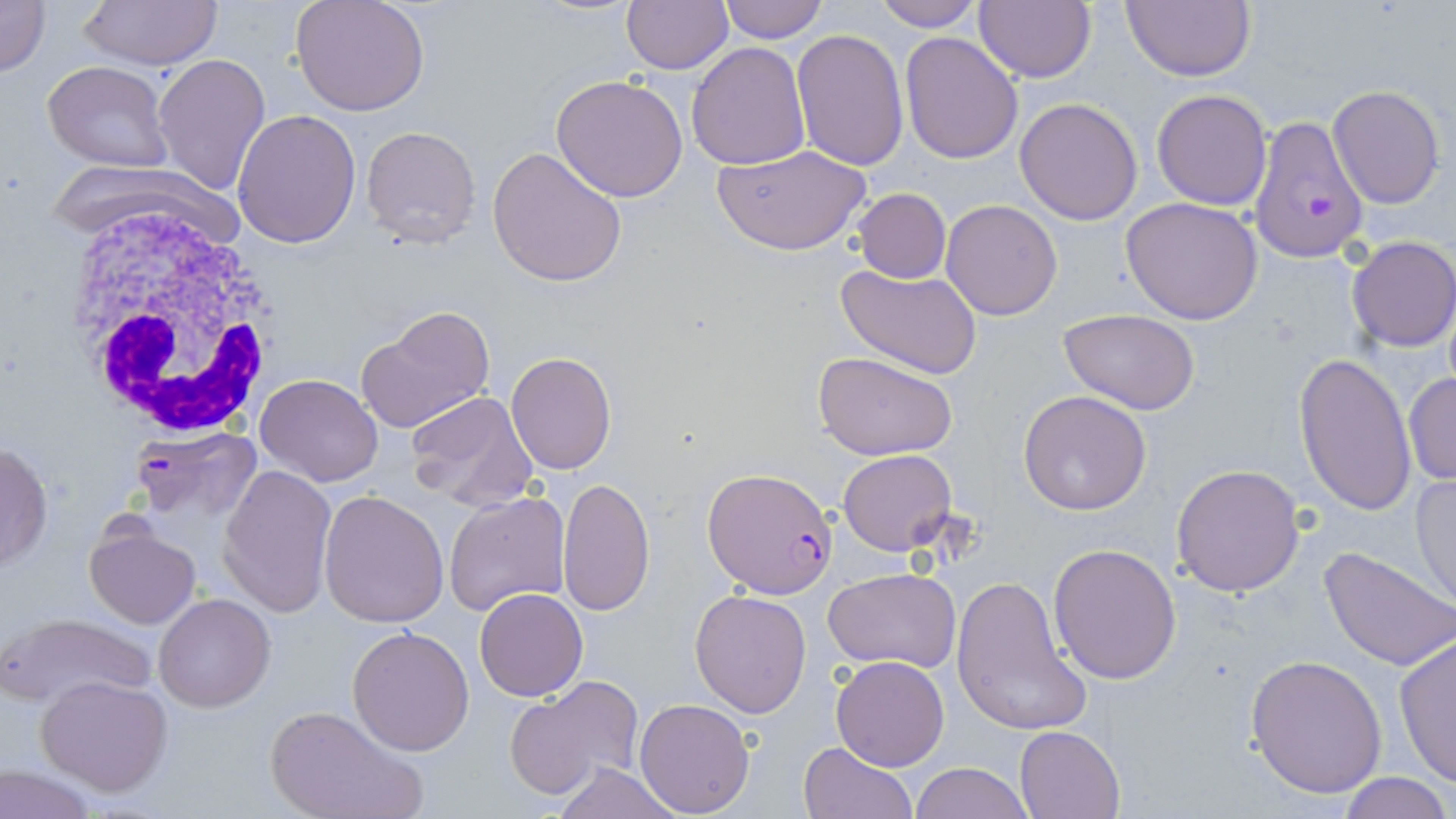

Summary:
  - Coordinate format: approximate bounding boxes as (x1,y1)-(x2,y2) corner pairs in pixels
  - White blood cell locations: (56,198)-(289,446)
  - Plasmodium falciparum-infected red blood cell locations: (1236,118)-(1367,261), (131,427)-(262,526), (702,465)-(839,599)
  - Uninfected red blood cell locations: (0,0)-(50,77), (77,0)-(221,70), (621,0)-(733,73), (716,0)-(832,44), (1123,0)-(1256,82), (291,1)-(431,116), (873,1)-(983,31), (975,2)-(1096,83), (791,29)-(909,170), (900,32)-(1023,164), (686,42)-(812,170), (152,54)-(272,197), (42,59)-(173,171), (550,75)-(689,202), (1327,84)-(1446,211), (1151,89)-(1272,210), (1015,97)-(1144,224), (232,110)-(362,249), (360,126)-(482,248), (712,142)-(872,256), (487,145)-(625,287), (852,187)-(951,285), (1121,196)-(1263,323), (940,199)-(1064,320), (1346,237)-(1456,353), (836,264)-(983,381), (355,308)-(496,435), (1059,309)-(1204,415), (812,350)-(959,459), (507,352)-(616,474), (1294,353)-(1418,518), (1402,373)-(1455,486), (255,374)-(384,487), (1018,389)-(1153,515), (405,390)-(540,510), (0,441)-(53,574), (837,449)-(957,556), (1172,462)-(1306,596), (218,465)-(337,617), (1409,472)-(1456,608), (557,477)-(656,617), (442,490)-(570,617), (318,491)-(449,628), (84,523)-(200,630), (1048,543)-(1182,685), (1318,545)-(1456,672), (825,568)-(961,673), (952,574)-(1090,736), (475,588)-(588,702), (690,588)-(813,718), (153,593)-(275,712), (3,610)-(156,708), (347,626)-(475,757), (1393,631)-(1456,788), (1246,654)-(1388,799), (830,656)-(949,771), (35,674)-(173,795), (504,676)-(645,800), (634,698)-(755,817), (264,703)-(426,819), (1015,726)-(1124,818), (799,741)-(917,819), (0,761)-(104,819), (909,761)-(1034,819), (549,762)-(685,819), (1337,773)-(1454,818)
  - Slide-level diagnosis: Plasmodium falciparum
  - Stain: May-Grünwald-Giemsa
  - Field of view: one of a larger specimen
  - Magnification: 1000x
  - Image size: 1456×819 pixels
  - Preparation: thin blood film
  - Modality: optical microscopy